Identify the parasite.
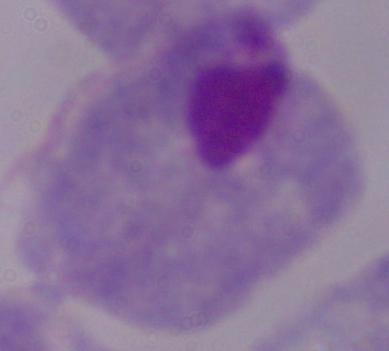

A trichomonad.

magnification = 1000x
modality = micrograph